Classify this cell by malaria status.
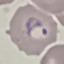
It is parasitized.

{
  "stain": "Giemsa",
  "preparation": "thin smear",
  "image_type": "automatically extracted cell patch, resized to 64 × 64 pixels",
  "capture": "smartphone camera at the microscope eyepiece"
}